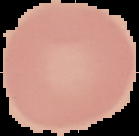 From a thin blood film. Malaria status: uninfected. Image is 139×136 pixels. Cell region segmented out of the field of view; the surrounding area is masked to black.